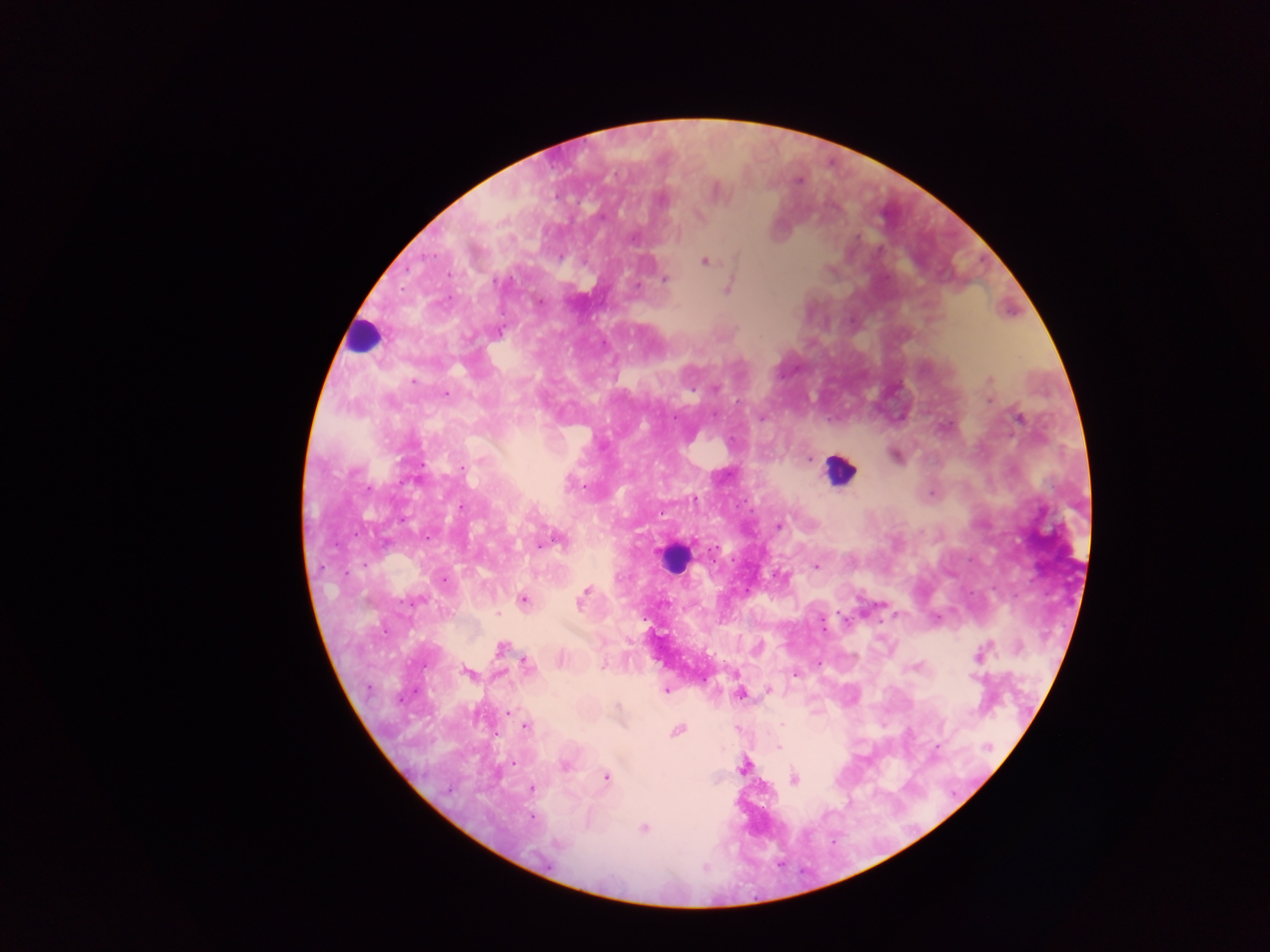
{
  "preparation": "thick blood film",
  "field_of_view": "single",
  "image_size": "1270×952 pixels",
  "country": "Ghana",
  "leukocyte_locations": "approximate centers as [x, y] in pixels: [362, 344], [844, 475], [677, 564]",
  "capture": "mobile-phone photograph through a microscope",
  "malaria_parasite_locations": "approximate centers as [x, y] in pixels: [798, 181], [717, 190], [704, 262], [647, 266], [666, 279], [727, 289], [537, 300], [989, 378], [716, 388], [448, 392], [735, 399], [991, 400], [762, 417], [1021, 418], [811, 456], [722, 476], [462, 506], [661, 511], [780, 526], [560, 542], [538, 546], [815, 566], [583, 598], [523, 599], [880, 605], [497, 614], [938, 616], [893, 617], [500, 648], [978, 654], [604, 662], [525, 663], [920, 664], [915, 667], [464, 672], [794, 676], [468, 677], [969, 677], [973, 680], [369, 689], [667, 690], [768, 691], [741, 694], [616, 705], [511, 711], [779, 725], [526, 727], [676, 732], [778, 748], [511, 761], [566, 768], [607, 777], [794, 781], [531, 788], [530, 818], [644, 829], [557, 842]"
}